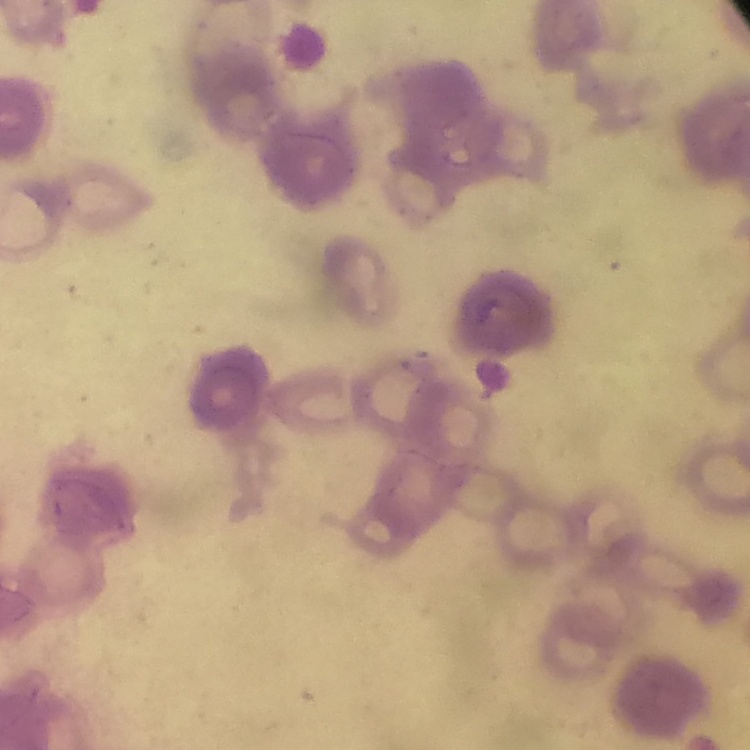
The red blood cells show rouleaux formation. Stained with either Field's or Giemsa. One tile cut from a larger photomicrograph. Thin peripheral smear.